Outline each white blood cell.
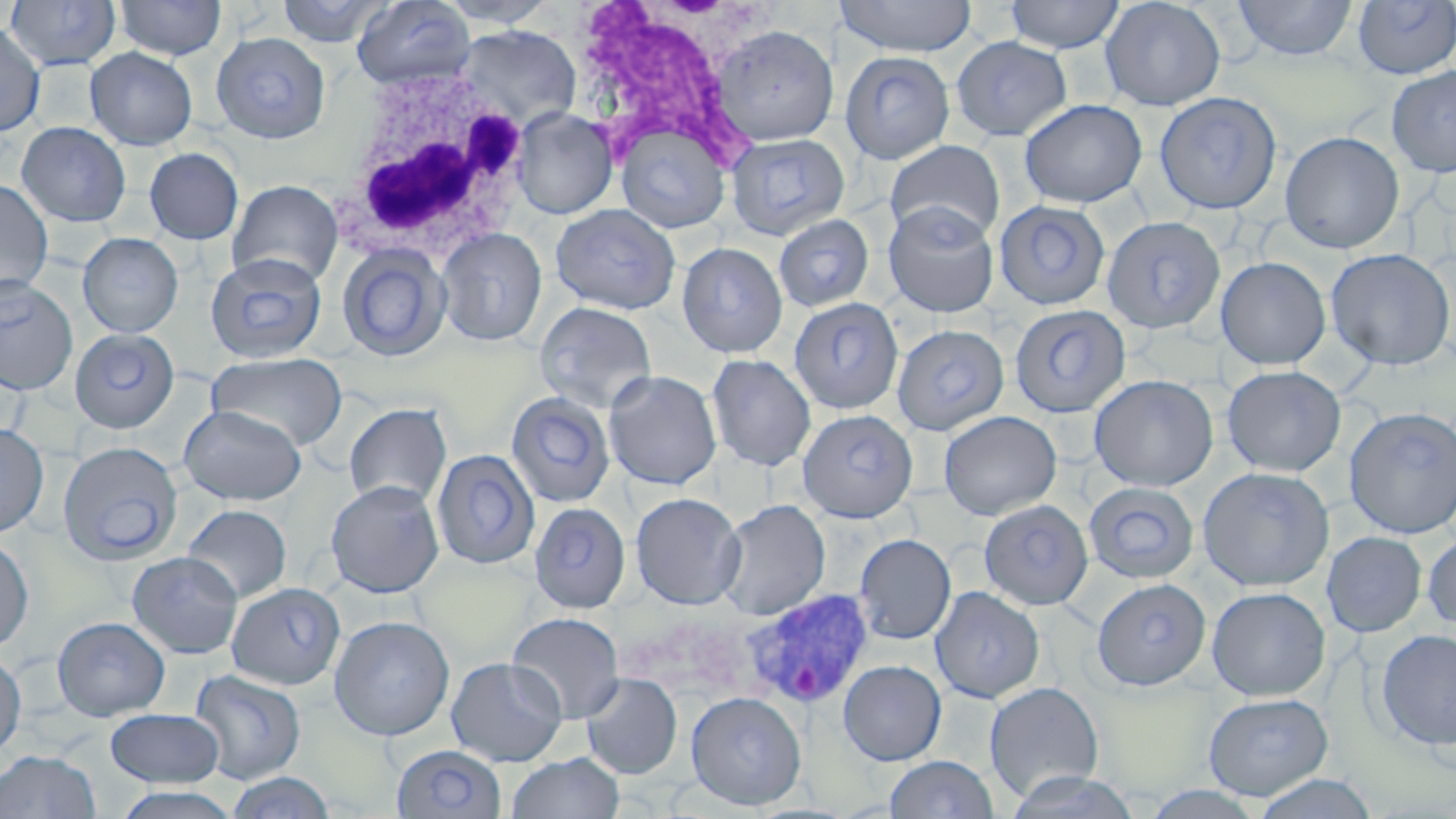
Approximate bounding boxes as (x1,y1)-(x2,y2) corner pairs in pixels.
White blood cells: (586,3)-(743,161), (336,64)-(534,262).

Plasmodium vivax-infected red blood cell locations: (739,588)-(875,710). Uninfected red blood cell locations: (115,0)-(227,60), (276,0)-(393,47), (351,0)-(476,90), (434,0)-(560,28), (834,0)-(977,57), (1003,0)-(1125,54), (1099,0)-(1226,111), (1230,0)-(1358,62), (3,1)-(122,70), (1353,1)-(1456,79), (0,22)-(45,136), (711,24)-(839,145), (455,25)-(581,128), (211,32)-(330,143), (950,37)-(1074,141), (85,47)-(198,150), (839,50)-(956,165), (1386,65)-(1456,177), (1153,92)-(1282,214), (1019,98)-(1147,208), (512,108)-(617,218), (16,121)-(132,227), (614,121)-(731,233), (1279,131)-(1405,253), (725,133)-(848,240), (884,140)-(1005,242), (143,147)-(244,245), (0,179)-(53,298), (227,179)-(343,286), (994,200)-(1110,310), (882,202)-(999,318), (550,204)-(681,315), (772,214)-(875,313), (1101,215)-(1226,334), (436,227)-(547,346), (78,232)-(183,337), (677,242)-(789,359), (336,244)-(453,363), (1325,248)-(1455,370), (205,254)-(328,364), (1215,256)-(1332,369), (0,278)-(78,394), (787,299)-(904,416), (534,301)-(658,413), (1010,304)-(1132,420), (893,323)-(1009,435), (70,328)-(179,433), (206,352)-(348,450), (705,353)-(817,471), (1222,365)-(1346,477), (603,370)-(723,490), (1089,374)-(1219,491), (505,391)-(616,508), (343,403)-(452,509), (178,405)-(307,505), (1343,406)-(1456,539), (798,410)-(918,522), (938,410)-(1062,520), (0,423)-(49,538), (58,441)-(183,565), (431,449)-(539,569), (1197,466)-(1334,592), (325,480)-(445,597), (1084,481)-(1200,584), (630,492)-(745,609), (716,499)-(830,620), (978,499)-(1094,610), (529,502)-(632,613), (182,504)-(292,603), (1423,529)-(1456,632), (1322,531)-(1427,637), (853,533)-(956,644), (0,536)-(34,652), (127,551)-(244,658), (1092,578)-(1211,690), (226,582)-(348,691), (1206,586)-(1331,701), (930,587)-(1045,704), (506,611)-(626,723), (329,615)-(455,740), (51,616)-(171,721), (1375,628)-(1456,750), (0,651)-(26,758), (446,656)-(568,766), (838,660)-(947,765), (188,668)-(307,784), (580,673)-(683,780), (984,681)-(1105,802), (685,691)-(806,810), (1202,692)-(1334,800), (106,709)-(225,787), (393,746)-(508,819), (0,749)-(101,818), (505,753)-(624,819), (884,755)-(999,818), (1002,771)-(1143,818), (223,772)-(336,818), (1251,774)-(1378,819), (108,786)-(244,819), (1140,786)-(1269,818). Slide-level diagnosis: Plasmodium vivax. Captured at 1000x magnification. Thin blood film. Image is 1456×819 pixels. May-Grünwald-Giemsa-stained preparation. Optical microscopy. Single field of view.